Point out each malaria parasite.
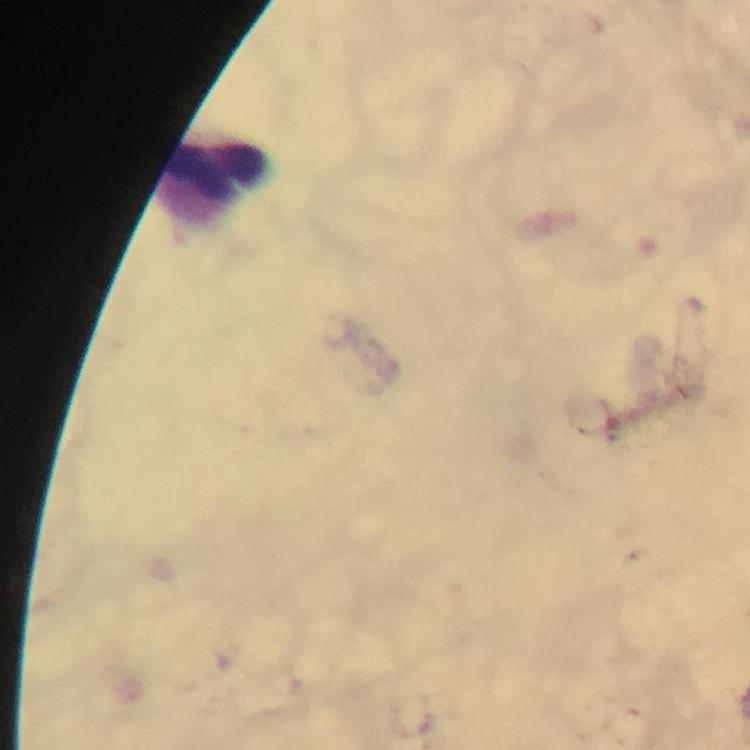
No malaria parasites detected.

{
  "capture": "smartphone camera through the microscope",
  "leukocyte_locations": "approximate centers as {x, y} in pixels: {218, 182}",
  "cropped_from": "a single field of view",
  "stain": "Giemsa",
  "immersion_oil": "applied",
  "image_size": "750×750 pixels",
  "magnification": "100x",
  "context": "from a diagnostic examination for malaria",
  "preparation": "thick blood smear"
}